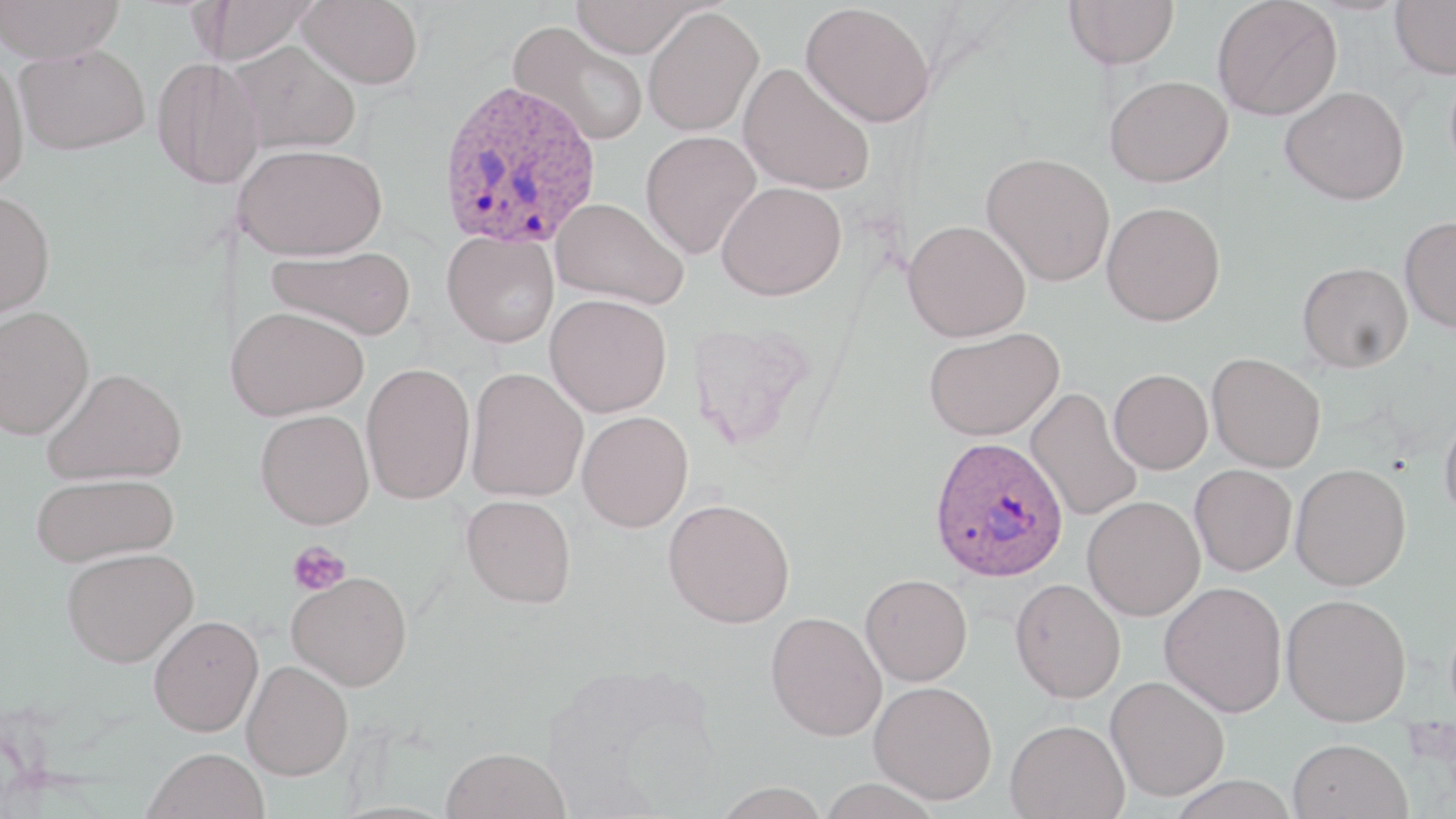
Plasmodium ovale-infected red blood cell locations = approximate bounding boxes as (x1,y1)-(x2,y2) corner pairs in pixels: (435,78)-(603,251), (928,436)-(1069,583)
slide-level diagnosis = Plasmodium ovale
stain = May-Grünwald-Giemsa
image size = 1456×819 pixels
field of view = one of a larger specimen
uninfected red blood cell locations = approximate bounding boxes as (x1,y1)-(x2,y2) corner pairs in pixels: (0,0)-(126,64), (199,0)-(318,64), (298,0)-(424,89), (568,0)-(703,58), (1064,0)-(1180,69), (1211,0)-(1342,120), (1390,0)-(1456,79), (801,2)-(936,128), (642,6)-(763,137), (508,21)-(648,147), (230,40)-(361,154), (14,44)-(150,155), (0,55)-(29,195), (151,57)-(264,189), (737,62)-(875,196), (1104,74)-(1233,187), (1280,85)-(1409,205), (640,130)-(761,259), (234,143)-(388,261), (981,151)-(1115,287), (716,180)-(847,301), (0,189)-(56,319), (552,197)-(689,308), (1101,201)-(1225,326), (1399,215)-(1456,334), (902,219)-(1031,342), (442,230)-(559,348), (267,244)-(416,340), (1297,261)-(1413,373), (545,293)-(672,416), (0,305)-(95,440), (225,305)-(368,421), (923,327)-(1063,441), (1207,352)-(1326,473), (361,362)-(475,504), (42,367)-(187,485), (465,367)-(588,502), (1108,368)-(1213,474), (1026,387)-(1142,521), (1439,406)-(1456,526), (255,409)-(375,529), (577,410)-(693,532), (1290,463)-(1411,590), (1190,464)-(1297,576), (30,472)-(178,567), (461,495)-(576,608), (1082,495)-(1205,621), (663,498)-(796,628), (61,547)-(199,666), (287,571)-(413,691), (860,573)-(973,686), (1010,577)-(1126,703), (1160,581)-(1287,717), (1281,593)-(1412,726), (765,611)-(887,741), (148,614)-(264,736), (242,660)-(353,780), (1106,675)-(1231,801), (869,680)-(998,805), (1005,718)-(1129,818), (1287,738)-(1412,819), (143,747)-(270,819), (441,747)-(571,819), (817,777)-(943,819), (711,781)-(831,818)
magnification = 1000x
preparation = thin blood smear
modality = optical microscopy
platelet locations = approximate bounding boxes as (x1,y1)-(x2,y2) corner pairs in pixels: (287,540)-(351,596)